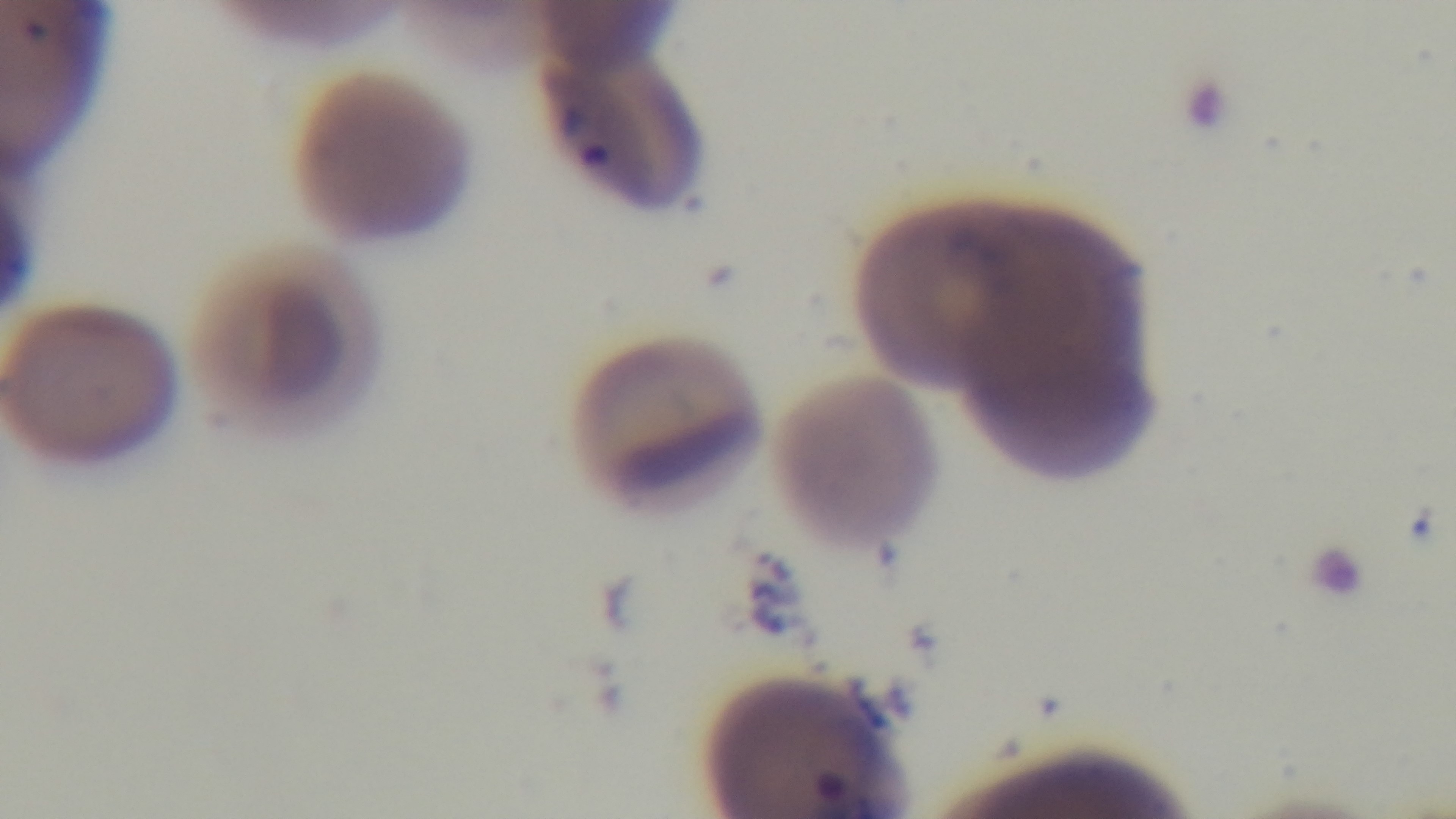

Giemsa stain. Preparation: thin. Captured with a mounted 4K digital camera. Malaria status: infected. One field from the slide. 100x oil-immersion objective. Light microscopy.